Mark where leukocytes are.
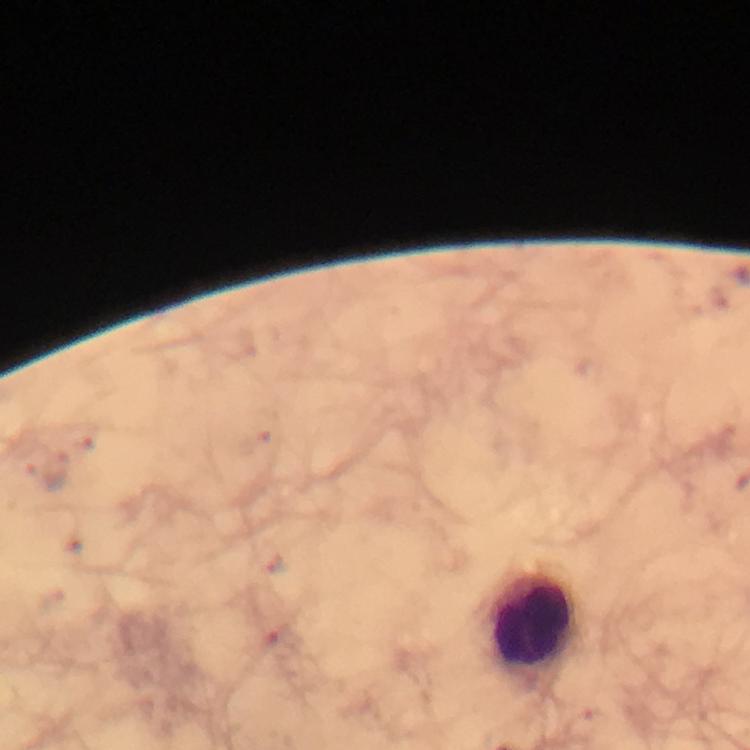

Approximate centers as {x, y} in pixels.
Leukocytes: {534, 623}.

Summary:
  - Plasmodium parasite locations: {49, 475}
  - Image size: 750×750 pixels
  - Stain: Giemsa
  - Capture: smartphone photograph through a microscope
  - Cropped from: a single field of view
  - Context: from a malaria diagnostic workup
  - Preparation: thick smear
  - Immersion oil: used
  - Magnification: 100x